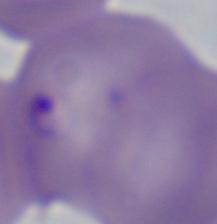
Summary:
  - Modality: micrograph
  - Magnification: 1000x
  - Identification: Babesia